Outline platelets.
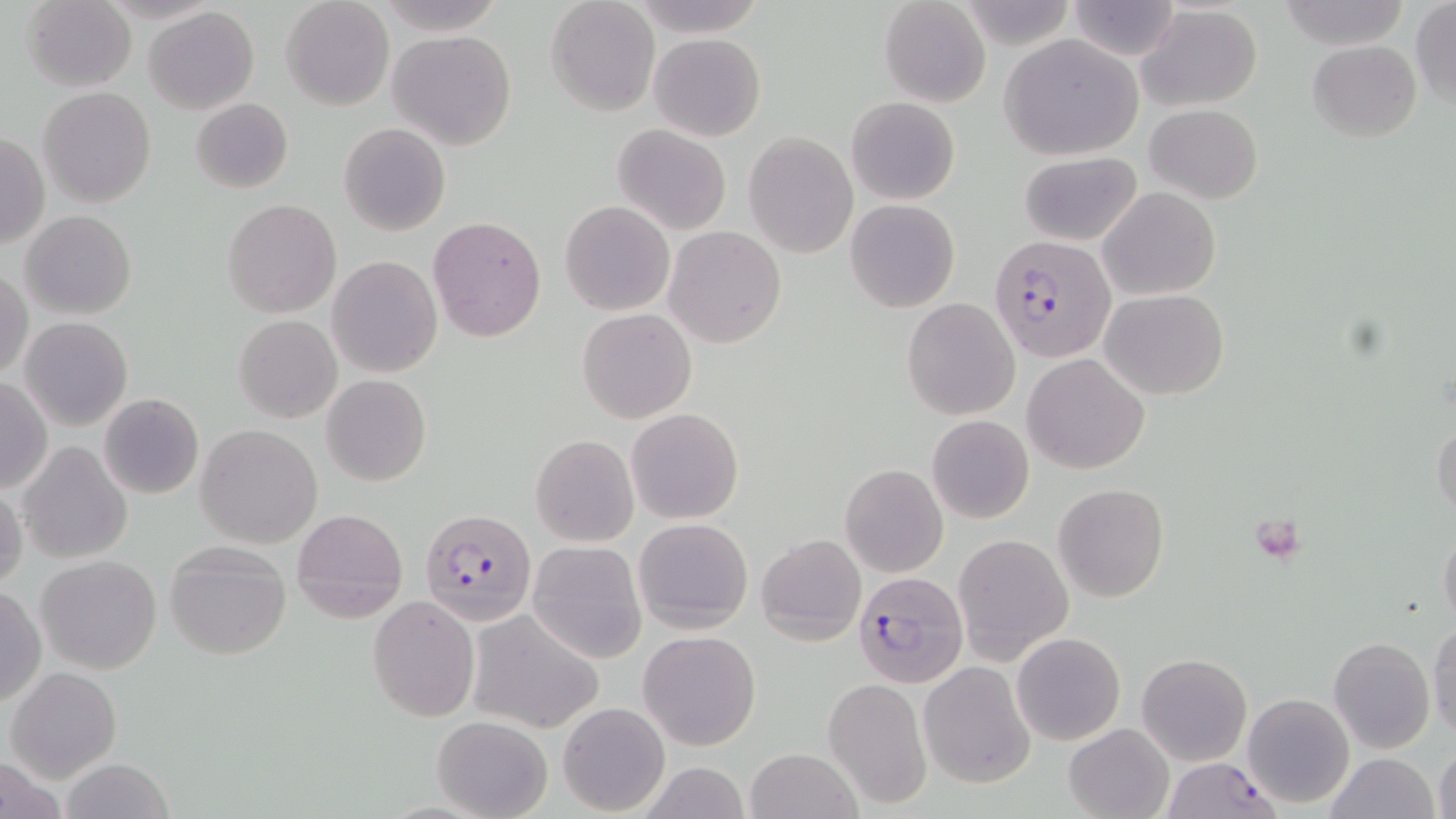
Approximate bounding boxes as (x1, y1, x2, y2) in pixels.
Platelets: (1259, 523, 1299, 562).

Summary:
  - Plasmodium falciparum-infected red blood cell locations: (990, 231, 1116, 362), (421, 508, 538, 626), (854, 571, 969, 688), (1158, 759, 1278, 819)
  - Uninfected red blood cell locations: (24, 0, 137, 91), (280, 0, 393, 111), (545, 1, 659, 116), (879, 1, 990, 108), (1065, 1, 1183, 62), (1278, 1, 1408, 47), (379, 2, 507, 35), (1410, 2, 1456, 109), (1137, 4, 1263, 111), (143, 6, 259, 115), (388, 29, 515, 150), (649, 32, 765, 141), (1000, 35, 1142, 160), (1307, 39, 1421, 142), (38, 88, 156, 208), (847, 96, 960, 205), (190, 98, 293, 193), (1146, 104, 1263, 203), (627, 119, 754, 336), (338, 122, 450, 236), (613, 124, 730, 236), (1, 131, 49, 252), (744, 132, 858, 258), (1017, 152, 1140, 247), (1098, 187, 1221, 301), (222, 199, 341, 318), (845, 199, 960, 313), (559, 201, 675, 316), (20, 211, 137, 319), (427, 216, 546, 341), (665, 225, 785, 348), (327, 256, 442, 378), (1, 269, 33, 380), (1103, 289, 1227, 400), (901, 298, 1020, 420), (577, 309, 697, 424), (233, 315, 341, 422), (20, 317, 133, 431), (1022, 354, 1148, 474), (321, 374, 431, 487), (0, 375, 51, 493), (98, 393, 204, 499), (627, 408, 744, 524), (925, 414, 1034, 525), (1431, 417, 1455, 521), (196, 424, 323, 548), (531, 434, 639, 547), (18, 440, 132, 566), (839, 464, 948, 577), (1, 483, 25, 592), (1053, 483, 1171, 602), (291, 508, 407, 619), (634, 518, 753, 634), (1439, 522, 1456, 632), (952, 533, 1073, 663), (756, 534, 866, 644), (528, 540, 647, 665), (163, 542, 294, 661), (36, 555, 162, 674), (0, 584, 46, 707), (367, 595, 480, 721), (468, 611, 603, 733), (1428, 621, 1456, 742), (639, 630, 761, 750), (1012, 632, 1125, 745), (1327, 638, 1435, 754), (1137, 653, 1252, 765), (918, 661, 1035, 788), (6, 666, 122, 783), (822, 677, 933, 812), (1242, 692, 1354, 807), (557, 702, 670, 816), (432, 715, 554, 819), (1063, 723, 1175, 819), (1433, 742, 1455, 819), (745, 747, 863, 819), (0, 752, 70, 819), (1325, 753, 1440, 819), (60, 758, 178, 818)
  - Slide-level diagnosis: Plasmodium falciparum
  - Modality: optical microscopy
  - Stain: May-Grünwald-Giemsa
  - Magnification: 1000x
  - Preparation: thin blood smear
  - Image size: 1456×819 pixels
  - Field of view: one of a larger specimen